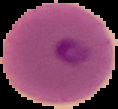
Summary:
  - Result: malaria parasites identified
  - Image size: 118×109 pixels
  - Image type: segmented cell region with the area outside set to black
  - Preparation: thin blood film